Assess this cell for malaria.
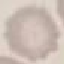
Uninfected.

image_type: automatically extracted cell patch, resized to 64 × 64 pixels
capture: smartphone camera at the microscope eyepiece
stain: Giemsa
preparation: thin smear